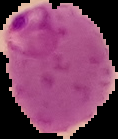 Malaria status: parasitized. Image is 118×139 pixels. From a thin blood film. Cell region segmented out of the field of view; the surrounding area is masked to black.